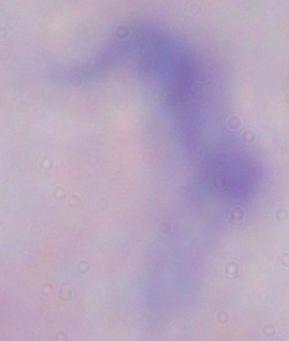
A trypanosome is seen. Micrograph. 1000x magnification.